Locate every blood parasite and identify its species.
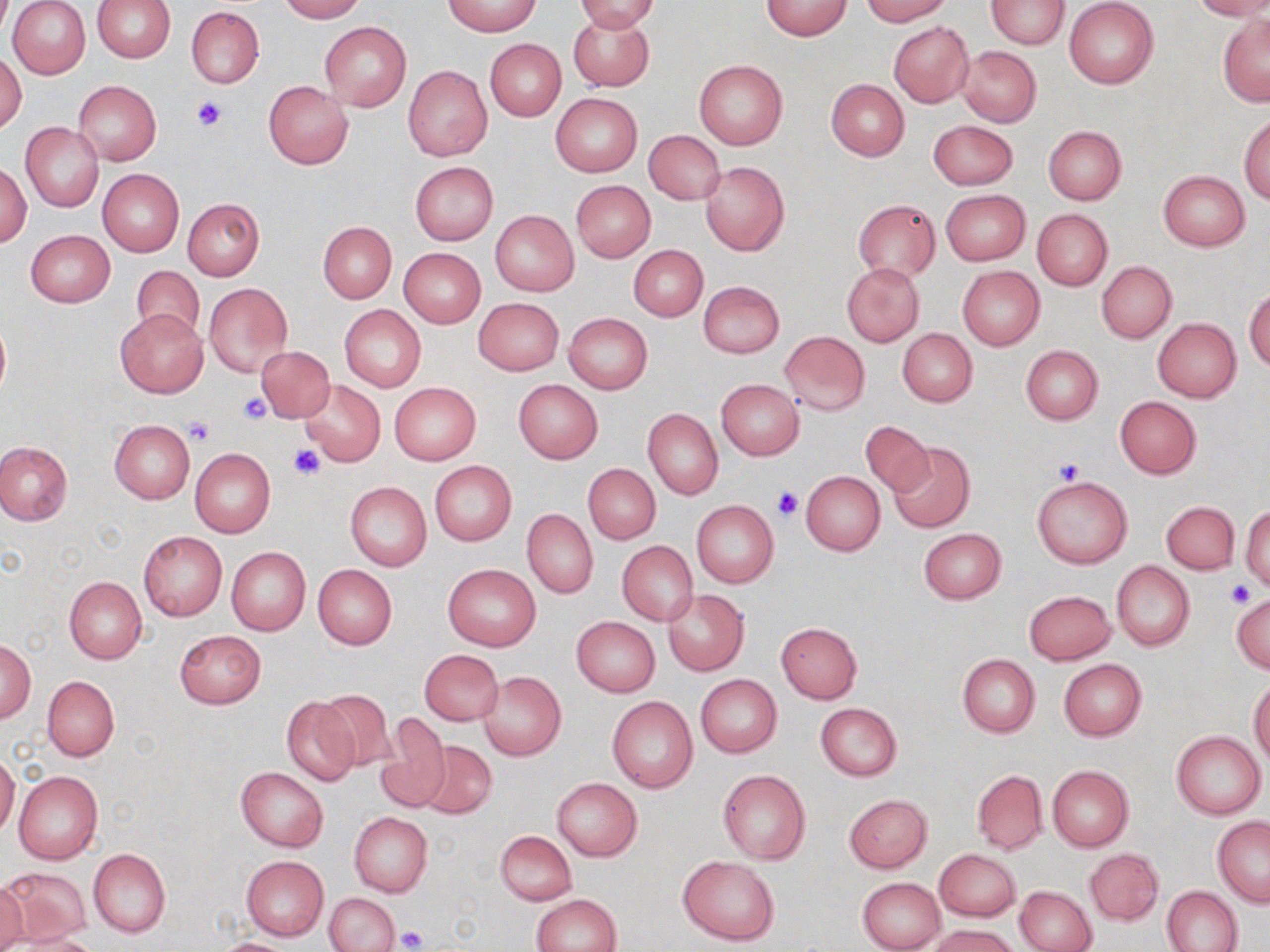
No blood parasites observed.

slide-level diagnosis = negative for blood parasites
platelet locations = approximate bounding boxes as named x1/y1/x2/y2 corners in pixels: (x1=193, y1=96, x2=227, y2=132), (x1=239, y1=392, x2=272, y2=424), (x1=185, y1=418, x2=215, y2=445), (x1=290, y1=445, x2=324, y2=479), (x1=1054, y1=457, x2=1084, y2=485), (x1=773, y1=486, x2=804, y2=521), (x1=1226, y1=580, x2=1254, y2=605), (x1=395, y1=927, x2=427, y2=952)
stain = May-Grünwald-Giemsa
image size = 1270×952 pixels
uninfected red blood cell locations = approximate bounding boxes as named x1/y1/x2/y2 corners in pixels: (x1=8, y1=0, x2=91, y2=80), (x1=92, y1=0, x2=176, y2=62), (x1=278, y1=0, x2=363, y2=22), (x1=574, y1=0, x2=660, y2=33), (x1=760, y1=0, x2=853, y2=40), (x1=862, y1=0, x2=951, y2=24), (x1=1190, y1=0, x2=1270, y2=20), (x1=444, y1=1, x2=540, y2=36), (x1=986, y1=1, x2=1069, y2=49), (x1=1064, y1=1, x2=1158, y2=88), (x1=187, y1=6, x2=263, y2=88), (x1=567, y1=10, x2=654, y2=91), (x1=1217, y1=13, x2=1269, y2=106), (x1=320, y1=21, x2=410, y2=111), (x1=888, y1=22, x2=974, y2=106), (x1=486, y1=39, x2=566, y2=120), (x1=956, y1=46, x2=1041, y2=127), (x1=0, y1=50, x2=27, y2=134), (x1=693, y1=59, x2=788, y2=150), (x1=403, y1=66, x2=492, y2=161), (x1=826, y1=78, x2=909, y2=160), (x1=73, y1=80, x2=161, y2=166), (x1=263, y1=82, x2=354, y2=169), (x1=551, y1=92, x2=643, y2=177), (x1=1240, y1=115, x2=1270, y2=203), (x1=929, y1=120, x2=1017, y2=189), (x1=20, y1=123, x2=103, y2=213), (x1=1042, y1=125, x2=1126, y2=205), (x1=643, y1=130, x2=725, y2=205), (x1=700, y1=161, x2=789, y2=256), (x1=410, y1=162, x2=498, y2=245), (x1=0, y1=163, x2=31, y2=246), (x1=98, y1=169, x2=183, y2=256), (x1=1159, y1=171, x2=1249, y2=250), (x1=571, y1=181, x2=654, y2=261), (x1=941, y1=189, x2=1030, y2=265), (x1=183, y1=198, x2=264, y2=280), (x1=853, y1=199, x2=939, y2=282), (x1=1032, y1=208, x2=1113, y2=290), (x1=490, y1=210, x2=579, y2=296), (x1=318, y1=221, x2=397, y2=303), (x1=26, y1=229, x2=114, y2=307), (x1=628, y1=245, x2=708, y2=321), (x1=398, y1=248, x2=486, y2=328), (x1=1096, y1=261, x2=1176, y2=343), (x1=842, y1=263, x2=924, y2=345), (x1=131, y1=265, x2=204, y2=342), (x1=957, y1=266, x2=1045, y2=350), (x1=698, y1=280, x2=785, y2=357), (x1=203, y1=283, x2=292, y2=376), (x1=1245, y1=286, x2=1270, y2=370), (x1=473, y1=297, x2=564, y2=376), (x1=340, y1=305, x2=426, y2=391), (x1=115, y1=309, x2=208, y2=399), (x1=564, y1=313, x2=652, y2=393), (x1=0, y1=317, x2=10, y2=403), (x1=1152, y1=318, x2=1241, y2=402), (x1=898, y1=328, x2=977, y2=407), (x1=779, y1=332, x2=871, y2=415), (x1=257, y1=345, x2=334, y2=423), (x1=1020, y1=345, x2=1103, y2=424), (x1=716, y1=378, x2=805, y2=459), (x1=513, y1=379, x2=603, y2=463), (x1=299, y1=380, x2=385, y2=467), (x1=389, y1=383, x2=480, y2=465), (x1=1114, y1=397, x2=1201, y2=479), (x1=642, y1=407, x2=723, y2=501), (x1=110, y1=420, x2=194, y2=504), (x1=860, y1=421, x2=932, y2=496), (x1=887, y1=440, x2=975, y2=533), (x1=0, y1=441, x2=73, y2=524), (x1=190, y1=449, x2=276, y2=539), (x1=429, y1=460, x2=517, y2=546), (x1=584, y1=464, x2=661, y2=543), (x1=802, y1=471, x2=885, y2=556), (x1=1032, y1=475, x2=1132, y2=567), (x1=345, y1=482, x2=431, y2=571), (x1=691, y1=500, x2=779, y2=588), (x1=1161, y1=501, x2=1239, y2=574), (x1=1242, y1=505, x2=1270, y2=591), (x1=522, y1=509, x2=598, y2=599), (x1=918, y1=528, x2=1006, y2=604), (x1=138, y1=531, x2=227, y2=621), (x1=616, y1=541, x2=698, y2=626), (x1=226, y1=546, x2=311, y2=636), (x1=1113, y1=561, x2=1194, y2=651), (x1=444, y1=563, x2=540, y2=651), (x1=313, y1=564, x2=397, y2=649), (x1=65, y1=577, x2=146, y2=665), (x1=1024, y1=590, x2=1116, y2=664), (x1=663, y1=591, x2=748, y2=675), (x1=1231, y1=593, x2=1270, y2=673), (x1=572, y1=616, x2=659, y2=696), (x1=775, y1=622, x2=863, y2=703), (x1=175, y1=630, x2=266, y2=708), (x1=1, y1=638, x2=35, y2=723), (x1=419, y1=649, x2=503, y2=726), (x1=956, y1=654, x2=1040, y2=737), (x1=1058, y1=659, x2=1147, y2=740), (x1=478, y1=671, x2=566, y2=760), (x1=696, y1=675, x2=782, y2=758), (x1=43, y1=676, x2=120, y2=761), (x1=1249, y1=677, x2=1270, y2=767), (x1=316, y1=689, x2=400, y2=770), (x1=283, y1=695, x2=361, y2=785), (x1=608, y1=696, x2=697, y2=793), (x1=816, y1=703, x2=901, y2=780), (x1=379, y1=716, x2=451, y2=809), (x1=1171, y1=731, x2=1266, y2=819), (x1=416, y1=740, x2=497, y2=820), (x1=0, y1=752, x2=20, y2=837), (x1=1047, y1=765, x2=1133, y2=852), (x1=235, y1=767, x2=329, y2=851), (x1=718, y1=770, x2=811, y2=865), (x1=972, y1=770, x2=1047, y2=854), (x1=14, y1=771, x2=103, y2=865), (x1=551, y1=777, x2=643, y2=861), (x1=844, y1=794, x2=932, y2=873), (x1=349, y1=812, x2=432, y2=896), (x1=1212, y1=817, x2=1270, y2=907), (x1=495, y1=831, x2=576, y2=905), (x1=89, y1=847, x2=170, y2=938), (x1=934, y1=849, x2=1021, y2=921), (x1=1085, y1=849, x2=1163, y2=924), (x1=241, y1=855, x2=328, y2=941), (x1=679, y1=855, x2=779, y2=945), (x1=1, y1=865, x2=90, y2=947), (x1=857, y1=877, x2=945, y2=952), (x1=0, y1=878, x2=29, y2=952), (x1=1163, y1=885, x2=1243, y2=952), (x1=1013, y1=886, x2=1096, y2=951), (x1=326, y1=892, x2=400, y2=952), (x1=531, y1=894, x2=621, y2=952), (x1=930, y1=924, x2=1021, y2=952), (x1=9, y1=934, x2=102, y2=952), (x1=210, y1=937, x2=304, y2=952)
magnification = 1000x
preparation = thin blood film
modality = light microscopy
field of view = single